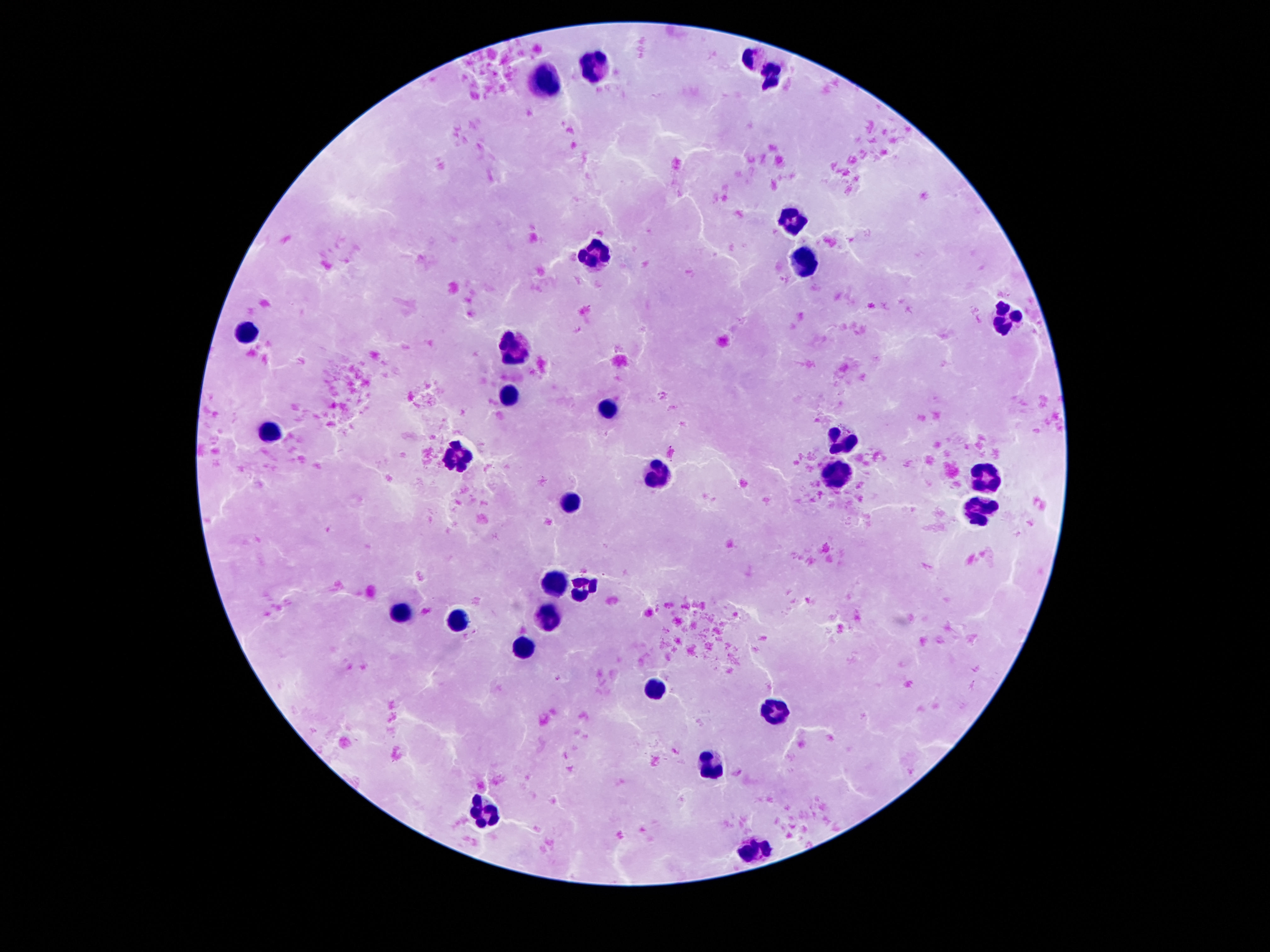

Approximate centers as [x, y] in pixels. Leukocyte locations: [754, 60], [592, 67], [770, 76], [548, 80], [790, 222], [596, 251], [804, 262], [1005, 317], [248, 330], [512, 347], [508, 393], [608, 411], [270, 432], [846, 441], [454, 455], [656, 476], [987, 478], [836, 479], [572, 501], [977, 513], [556, 580], [584, 586], [404, 612], [460, 619], [552, 619], [524, 647], [652, 690], [776, 709], [712, 767], [486, 814], [754, 849]. Image is 1270×952 pixels. One field from this slide. Smartphone photograph taken through the microscope eyepiece. Patient malaria status: not infected. Thick peripheral-blood smear. Giemsa-stained preparation. 100x magnification.